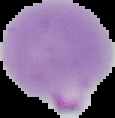 Malaria status: parasitized. Segmented cell region on a black background. From a thin blood film. Image is 115×118 pixels.